Identify the blood parasite species.
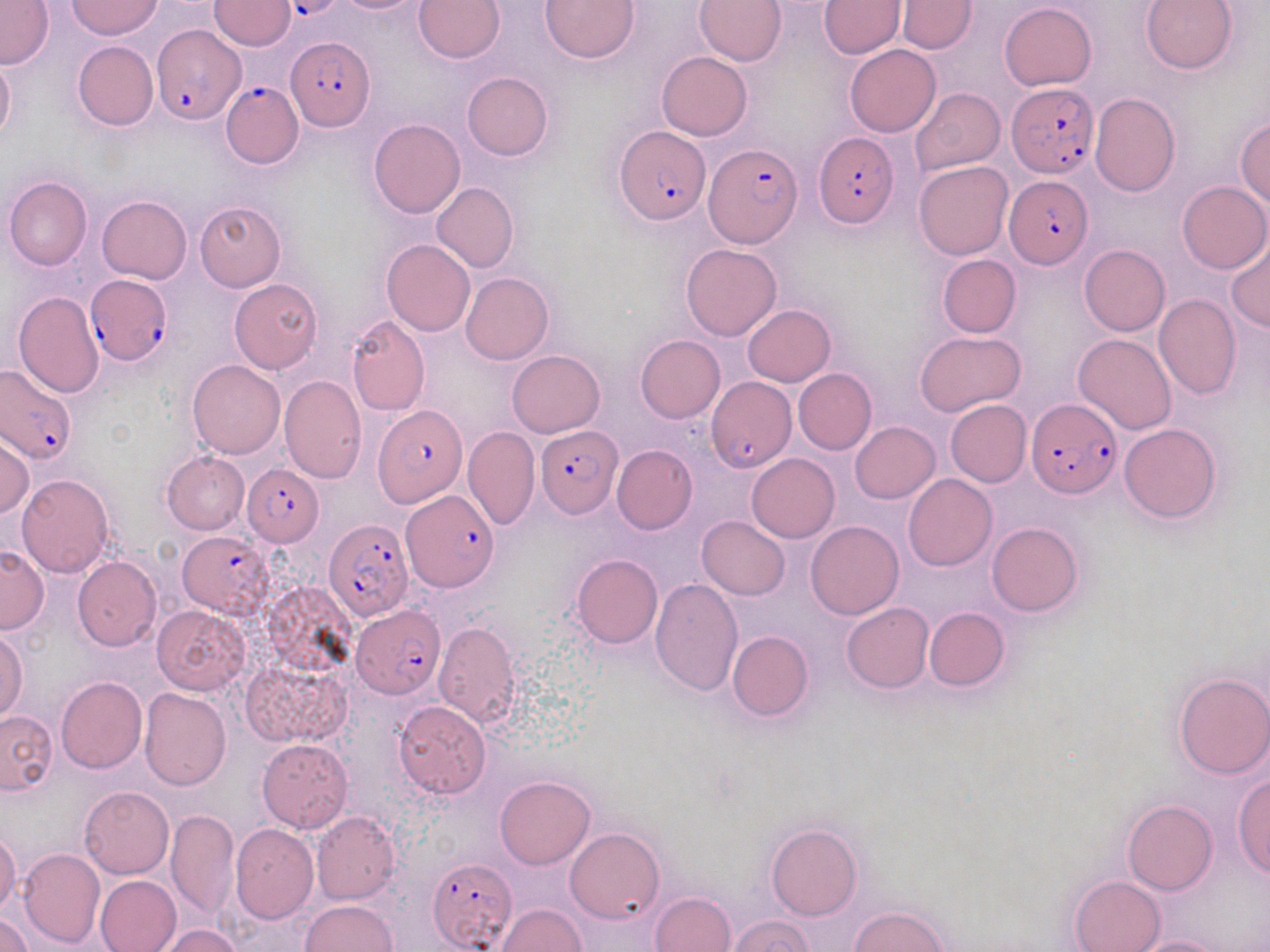

Plasmodium falciparum.

Summary:
  - Coordinate format: approximate bounding boxes as [x1, y1, x2, y2] in pixels
  - Uninfected red blood cell locations: [329, 0, 428, 14], [414, 0, 506, 63], [540, 0, 640, 64], [695, 0, 786, 66], [898, 0, 976, 54], [1140, 0, 1238, 74], [0, 1, 54, 70], [67, 1, 161, 40], [209, 1, 295, 51], [817, 1, 906, 58], [999, 3, 1096, 90], [73, 41, 158, 130], [845, 45, 940, 137], [0, 52, 15, 142], [655, 52, 752, 141], [462, 72, 553, 161], [911, 87, 1005, 176], [1088, 93, 1179, 197], [1235, 117, 1270, 207], [368, 119, 465, 218], [913, 161, 1013, 260], [3, 175, 92, 270], [430, 181, 519, 273], [1177, 181, 1270, 273], [97, 195, 191, 283], [194, 201, 286, 292], [381, 238, 475, 335], [1226, 239, 1269, 333], [681, 243, 782, 341], [1079, 244, 1170, 336], [937, 254, 1021, 338], [461, 273, 554, 364], [229, 278, 323, 373], [12, 291, 104, 398], [1153, 293, 1241, 399], [742, 304, 836, 386], [346, 314, 430, 415], [915, 330, 1027, 418], [1074, 334, 1176, 435], [635, 335, 725, 423], [506, 350, 606, 437], [186, 360, 285, 459], [793, 368, 876, 455], [279, 375, 366, 484], [945, 399, 1032, 486], [850, 421, 939, 503], [1118, 422, 1221, 523], [463, 427, 540, 531], [0, 434, 33, 521], [612, 444, 697, 534], [161, 451, 250, 534], [746, 454, 840, 543], [15, 473, 115, 578], [903, 473, 996, 570], [697, 515, 790, 599], [805, 520, 904, 620], [987, 521, 1083, 616], [0, 547, 50, 634], [570, 554, 663, 648], [73, 556, 162, 652], [649, 578, 743, 696], [840, 601, 933, 693], [151, 604, 249, 694], [923, 607, 1009, 691], [432, 620, 522, 730], [0, 629, 28, 722], [727, 630, 813, 722], [243, 658, 353, 747], [1173, 672, 1270, 779], [56, 677, 147, 774], [138, 687, 231, 789], [392, 700, 490, 798], [0, 710, 58, 794], [257, 739, 353, 833], [1231, 774, 1270, 878], [494, 775, 595, 869], [80, 786, 173, 879], [1122, 800, 1217, 895], [165, 808, 240, 921], [311, 811, 399, 906], [765, 823, 862, 921], [230, 824, 318, 924], [567, 827, 664, 923], [1, 830, 21, 916], [16, 847, 105, 948], [95, 875, 181, 952], [1070, 875, 1165, 952], [649, 891, 738, 952], [298, 900, 397, 952], [498, 904, 587, 951], [850, 906, 947, 952], [1, 912, 35, 952], [727, 916, 815, 952], [160, 925, 242, 952], [1129, 936, 1228, 952]
  - Plasmodium falciparum-infected red blood cell locations: [291, 1, 335, 21], [152, 21, 248, 129], [285, 37, 375, 131], [219, 80, 303, 168], [1005, 83, 1101, 178], [614, 128, 709, 224], [813, 134, 899, 227], [704, 144, 801, 247], [1003, 175, 1093, 269], [84, 275, 173, 367], [0, 365, 77, 465], [708, 378, 796, 473], [1027, 401, 1120, 499], [373, 404, 467, 508], [536, 425, 623, 518], [240, 462, 323, 546], [401, 490, 500, 591], [323, 518, 414, 620], [176, 532, 271, 618], [351, 606, 444, 700], [427, 859, 516, 951]
  - Magnification: 1000x
  - Modality: light microscopy
  - Image size: 1270×952 pixels
  - Stain: May-Grünwald-Giemsa
  - Field of view: one of a larger specimen
  - Preparation: thin blood smear